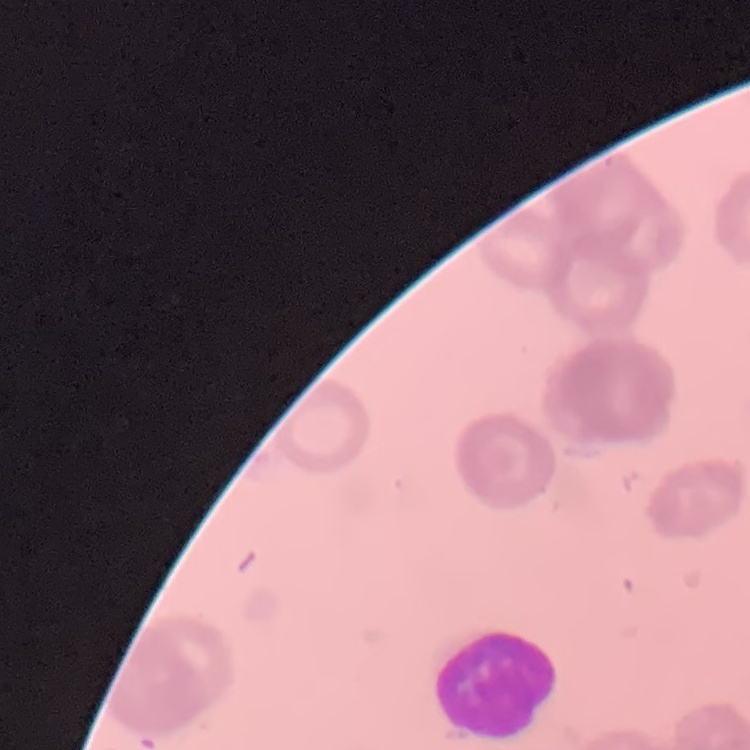

erythrocyte morphology = rouleaux formation
stain = Field's or Giemsa
preparation = thin peripheral smear
image type = square crop of a larger photomicrograph